Locate every Plasmodium parasite.
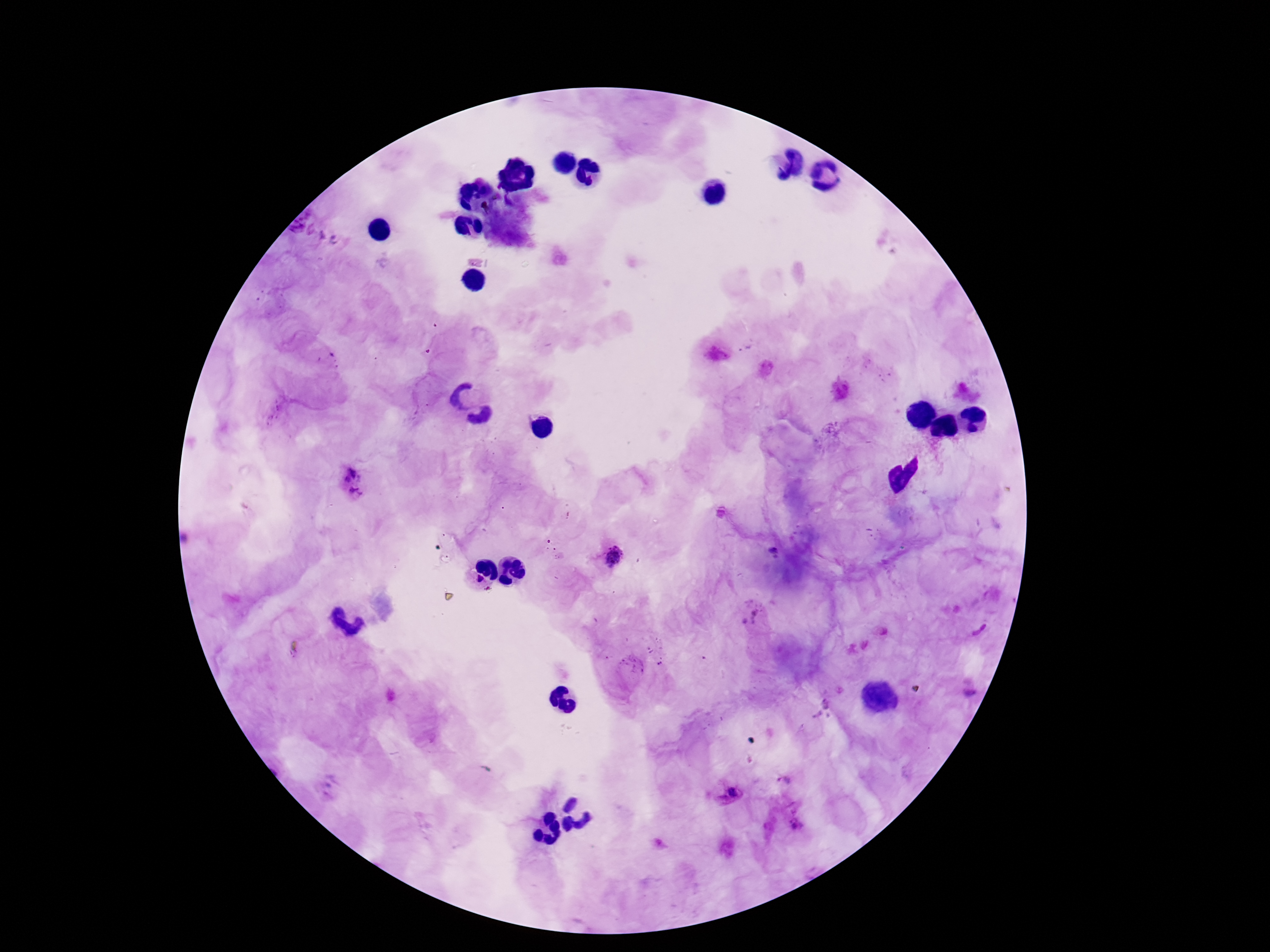
Approximate object centers, in pixels from the top-left corner.
Plasmodium parasites: (x=352, y=483), (x=774, y=553), (x=612, y=556), (x=475, y=584), (x=755, y=620), (x=971, y=693), (x=783, y=781), (x=730, y=794), (x=794, y=824).

Image is 1270×952 pixels. Smartphone photograph taken through the microscope eyepiece. Thick blood film. Patient malaria status: infected. 100x magnification. Single field of view. Giemsa-stained preparation.